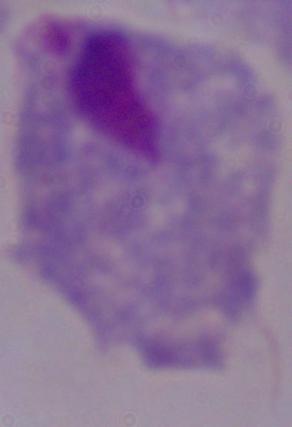
Summary:
  - Identification: trichomonad
  - Modality: micrograph
  - Magnification: 1000x